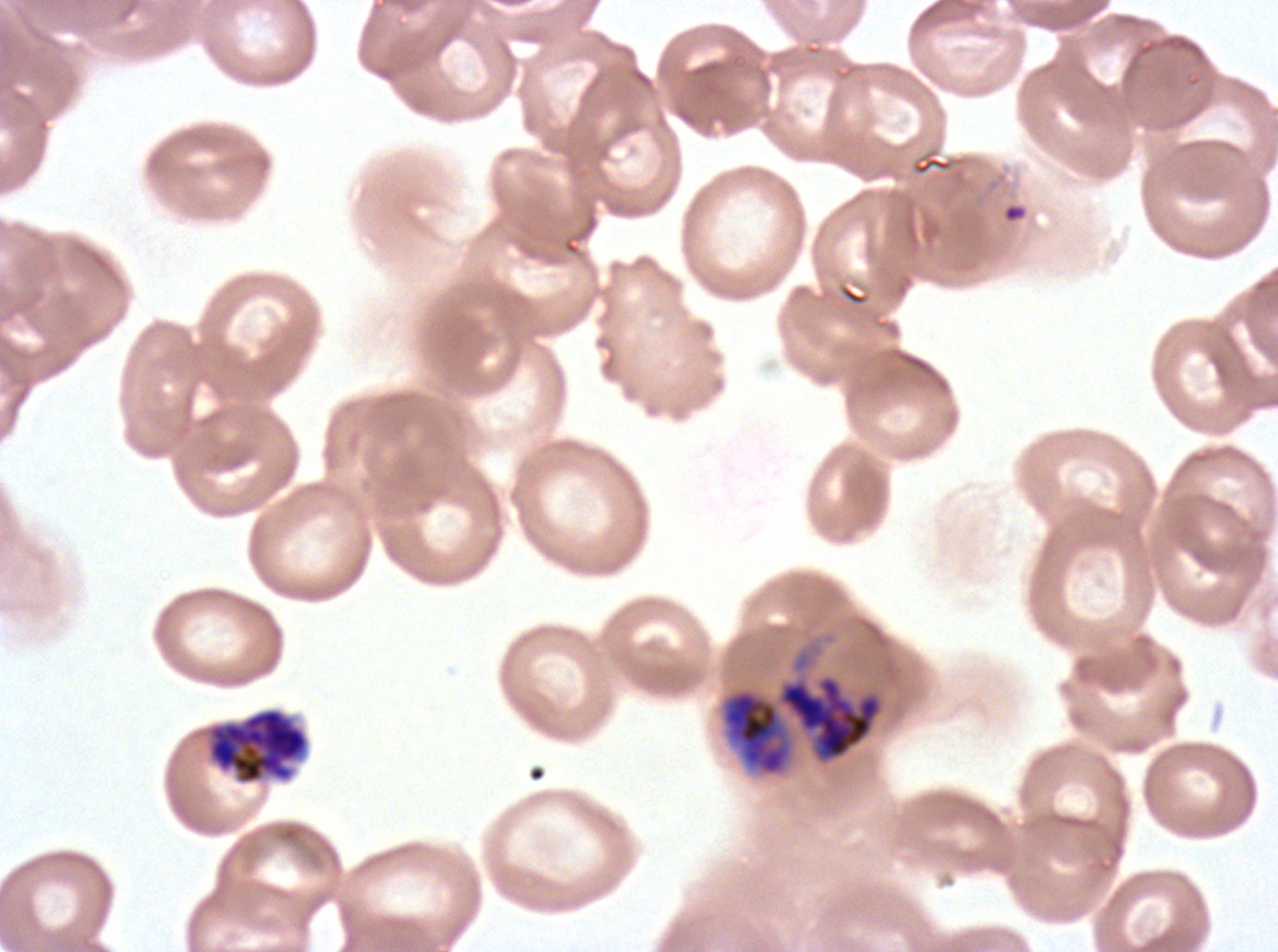
notation = approximate bounding rectangles given as corner coordinates in pixels from the top-left
debris locations = (x1=1002, y1=202, x2=1027, y2=224)
early schizont locations = (x1=780, y1=677, x2=881, y2=759), (x1=721, y1=689, x2=792, y2=776), (x1=208, y1=708, x2=308, y2=784)
specimen = P. falciparum cultured ex vivo for 24 to 48 hours, from a patient in The Gambia
stain = Giemsa
field of view = sub-image separated from a larger composite
image size = 1278×952 pixels
preparation = thin blood smear